Evaluate for malaria.
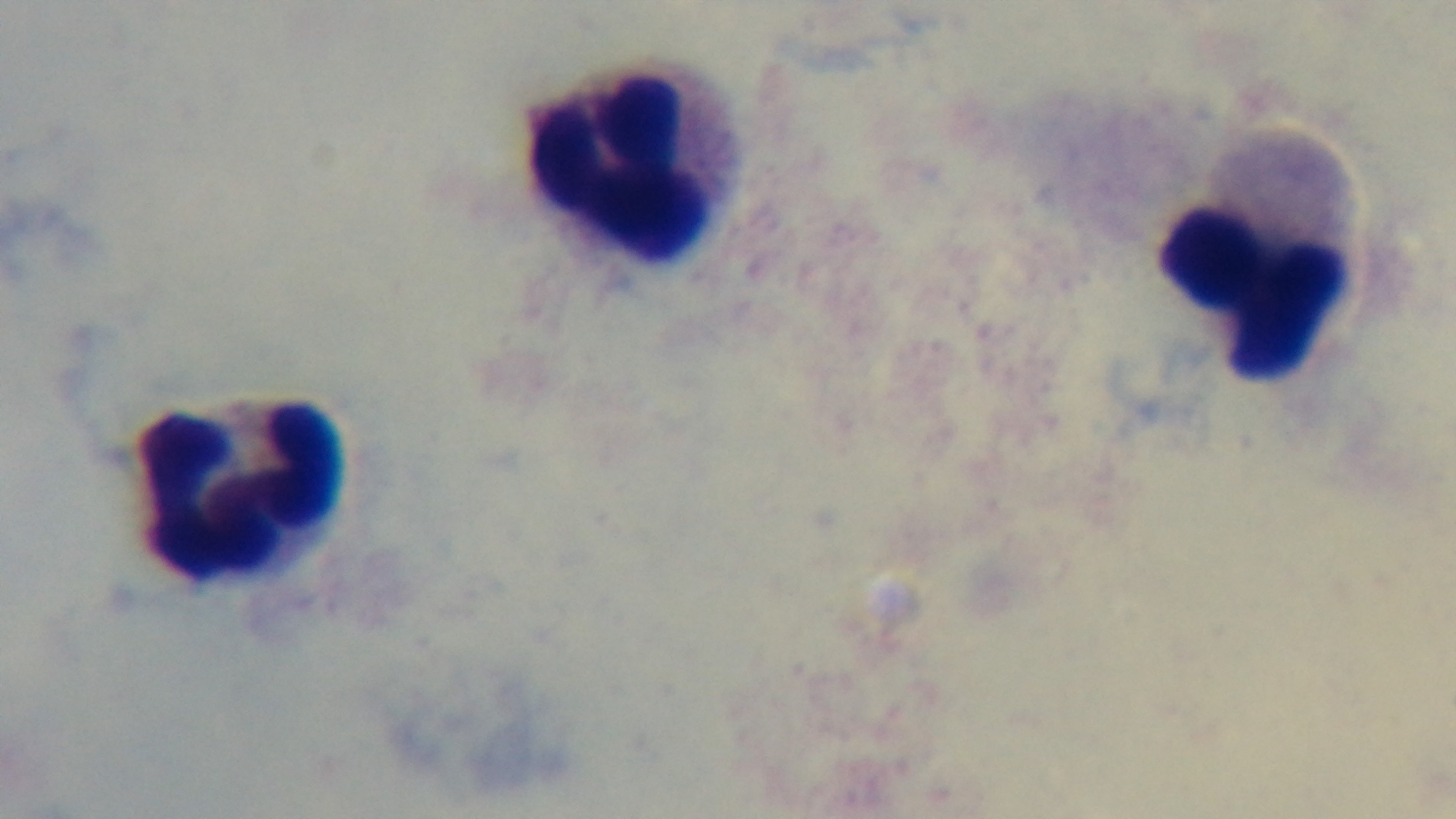
It is uninfected.

Light microscopy. 100x oil-immersion objective. Single field of view. Giemsa-stained. Captured with a mounted 4K digital camera. Preparation: thick blood film.